Locate platelets.
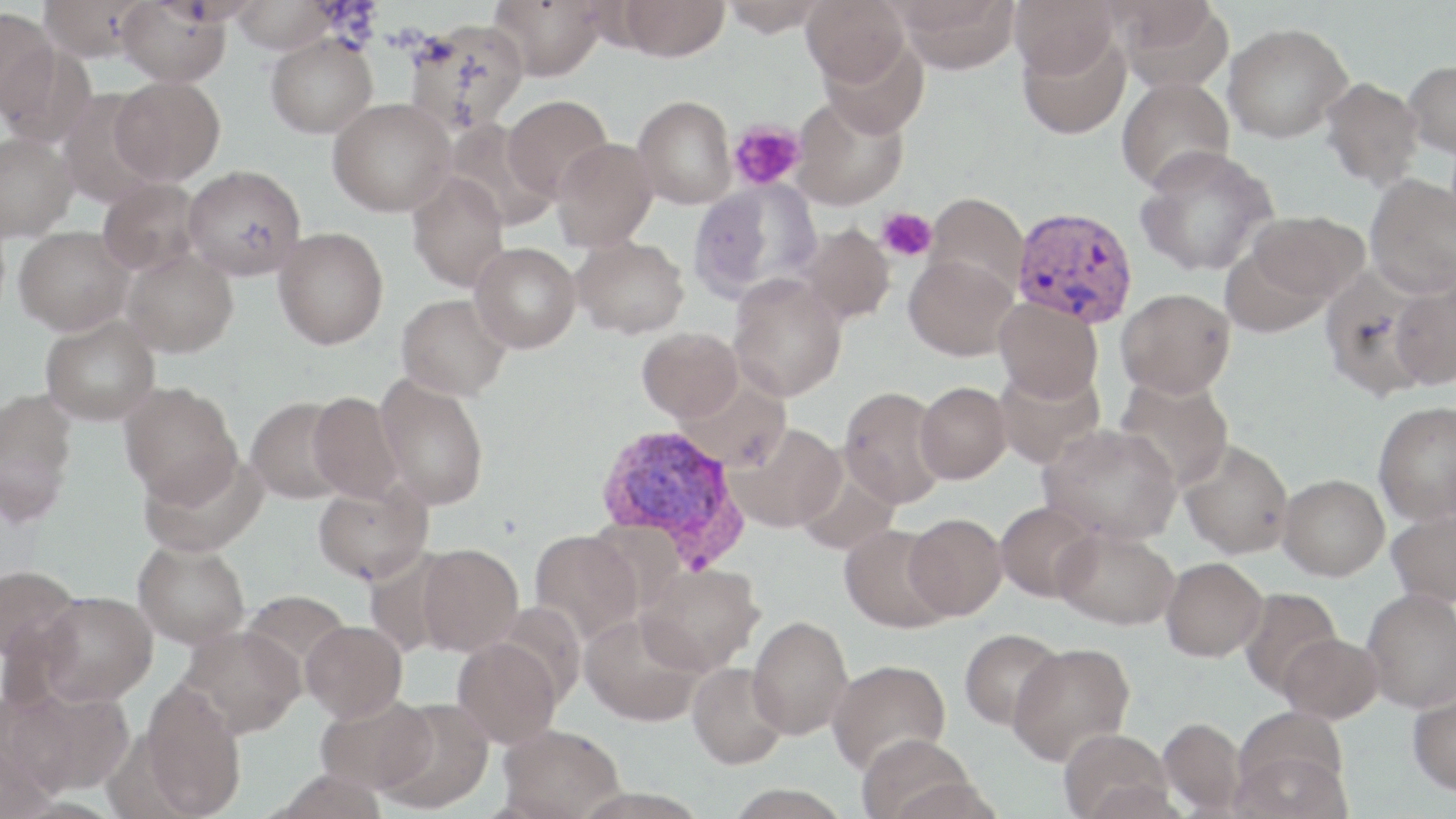

Approximate bounding boxes as named x1/y1/x2/y2 corners in pixels.
Platelets: (x1=728, y1=120, x2=805, y2=190), (x1=877, y1=207, x2=937, y2=262).

slide-level diagnosis = Plasmodium vivax
modality = light microscopy
stain = May-Grünwald-Giemsa
magnification = 1000x
uninfected red blood cell locations = approximate bounding boxes as named x1/y1/x2/y2 corners in pixels: (x1=38, y1=0, x2=148, y2=61), (x1=116, y1=0, x2=231, y2=87), (x1=230, y1=0, x2=336, y2=53), (x1=488, y1=0, x2=607, y2=80), (x1=720, y1=0, x2=830, y2=37), (x1=802, y1=0, x2=910, y2=86), (x1=893, y1=0, x2=1021, y2=74), (x1=1010, y1=0, x2=1119, y2=81), (x1=616, y1=1, x2=730, y2=61), (x1=1113, y1=2, x2=1232, y2=91), (x1=0, y1=8, x2=59, y2=120), (x1=405, y1=18, x2=530, y2=135), (x1=1223, y1=22, x2=1353, y2=143), (x1=1017, y1=29, x2=1131, y2=139), (x1=266, y1=33, x2=378, y2=138), (x1=1, y1=43, x2=97, y2=148), (x1=1404, y1=60, x2=1456, y2=158), (x1=110, y1=76, x2=225, y2=186), (x1=1117, y1=77, x2=1235, y2=194), (x1=1320, y1=77, x2=1423, y2=189), (x1=502, y1=95, x2=613, y2=202), (x1=633, y1=95, x2=737, y2=209), (x1=792, y1=95, x2=909, y2=211), (x1=328, y1=97, x2=455, y2=216), (x1=444, y1=120, x2=558, y2=230), (x1=0, y1=132, x2=78, y2=241), (x1=551, y1=137, x2=657, y2=251), (x1=1135, y1=145, x2=1279, y2=277), (x1=183, y1=164, x2=307, y2=280), (x1=406, y1=173, x2=510, y2=292), (x1=1365, y1=174, x2=1456, y2=298), (x1=97, y1=178, x2=205, y2=277), (x1=689, y1=179, x2=821, y2=301), (x1=925, y1=192, x2=1028, y2=298), (x1=1244, y1=210, x2=1370, y2=307), (x1=797, y1=223, x2=896, y2=325), (x1=14, y1=226, x2=134, y2=335), (x1=274, y1=227, x2=389, y2=349), (x1=573, y1=236, x2=690, y2=339), (x1=470, y1=241, x2=581, y2=353), (x1=1219, y1=243, x2=1334, y2=339), (x1=121, y1=248, x2=238, y2=357), (x1=904, y1=254, x2=1018, y2=361), (x1=1319, y1=266, x2=1437, y2=400), (x1=728, y1=276, x2=848, y2=400), (x1=1390, y1=277, x2=1456, y2=390), (x1=1117, y1=288, x2=1236, y2=398), (x1=396, y1=293, x2=511, y2=400), (x1=995, y1=297, x2=1103, y2=403), (x1=40, y1=314, x2=160, y2=425), (x1=637, y1=327, x2=743, y2=423), (x1=994, y1=365, x2=1105, y2=470), (x1=375, y1=374, x2=489, y2=510), (x1=1114, y1=374, x2=1235, y2=491), (x1=679, y1=380, x2=791, y2=472), (x1=119, y1=381, x2=241, y2=504), (x1=915, y1=381, x2=1012, y2=484), (x1=839, y1=386, x2=948, y2=508), (x1=0, y1=389, x2=78, y2=520), (x1=308, y1=391, x2=403, y2=502), (x1=246, y1=396, x2=351, y2=504), (x1=1373, y1=401, x2=1456, y2=525), (x1=729, y1=423, x2=845, y2=533), (x1=1039, y1=423, x2=1182, y2=544), (x1=1179, y1=440, x2=1294, y2=559), (x1=140, y1=448, x2=267, y2=557), (x1=1278, y1=473, x2=1389, y2=580), (x1=312, y1=479, x2=433, y2=584), (x1=995, y1=500, x2=1102, y2=602), (x1=1387, y1=507, x2=1456, y2=607), (x1=903, y1=513, x2=1007, y2=620), (x1=840, y1=524, x2=953, y2=633), (x1=1053, y1=527, x2=1179, y2=630), (x1=530, y1=530, x2=643, y2=643), (x1=133, y1=539, x2=250, y2=649), (x1=417, y1=543, x2=523, y2=656), (x1=1161, y1=556, x2=1267, y2=661), (x1=0, y1=563, x2=82, y2=669), (x1=637, y1=563, x2=763, y2=676), (x1=1239, y1=587, x2=1343, y2=697), (x1=1362, y1=588, x2=1456, y2=712), (x1=240, y1=590, x2=353, y2=680), (x1=37, y1=591, x2=158, y2=705), (x1=580, y1=612, x2=704, y2=726), (x1=748, y1=615, x2=854, y2=739), (x1=301, y1=620, x2=407, y2=722), (x1=180, y1=625, x2=305, y2=738), (x1=959, y1=628, x2=1066, y2=730), (x1=1278, y1=632, x2=1383, y2=723), (x1=453, y1=637, x2=562, y2=748), (x1=1008, y1=642, x2=1135, y2=765), (x1=827, y1=659, x2=951, y2=775), (x1=687, y1=661, x2=789, y2=770), (x1=138, y1=685, x2=246, y2=818), (x1=6, y1=688, x2=130, y2=798), (x1=1408, y1=688, x2=1456, y2=796), (x1=315, y1=693, x2=436, y2=795), (x1=377, y1=698, x2=494, y2=814), (x1=1158, y1=717, x2=1247, y2=815), (x1=1232, y1=721, x2=1351, y2=819), (x1=498, y1=724, x2=625, y2=819), (x1=1058, y1=729, x2=1172, y2=819), (x1=856, y1=733, x2=976, y2=819), (x1=270, y1=769, x2=388, y2=819)
Plasmodium vivax-infected red blood cell locations = approximate bounding boxes as named x1/y1/x2/y2 corners in pixels: (x1=1011, y1=206, x2=1138, y2=328), (x1=594, y1=423, x2=748, y2=567)
image size = 1456×819 pixels
preparation = thin blood smear
field of view = single